Describe the morphology of the erythrocytes.
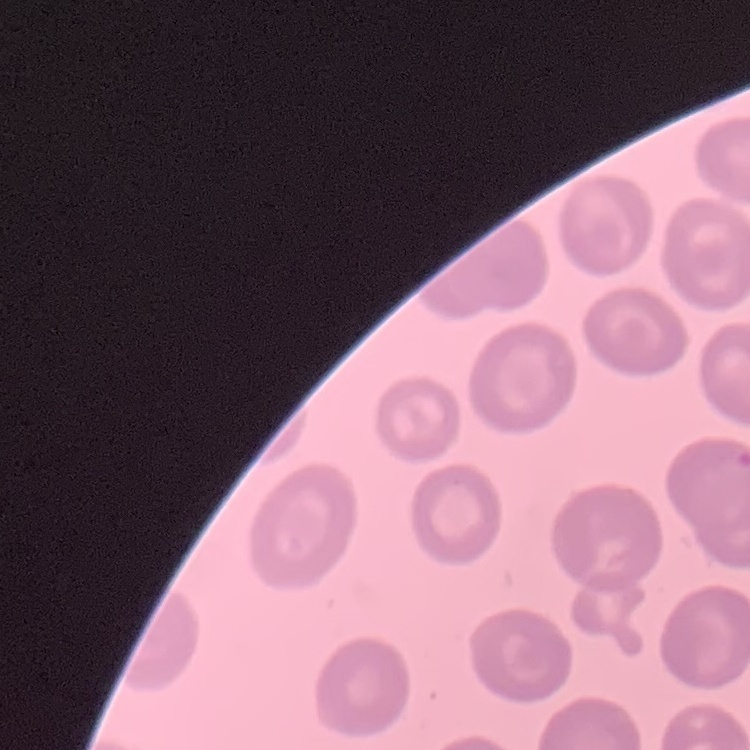

They show no rouleaux formation.

Summary:
  - Preparation: thin blood smear
  - Stain: Field's or Giemsa
  - Image type: square crop of a larger photomicrograph